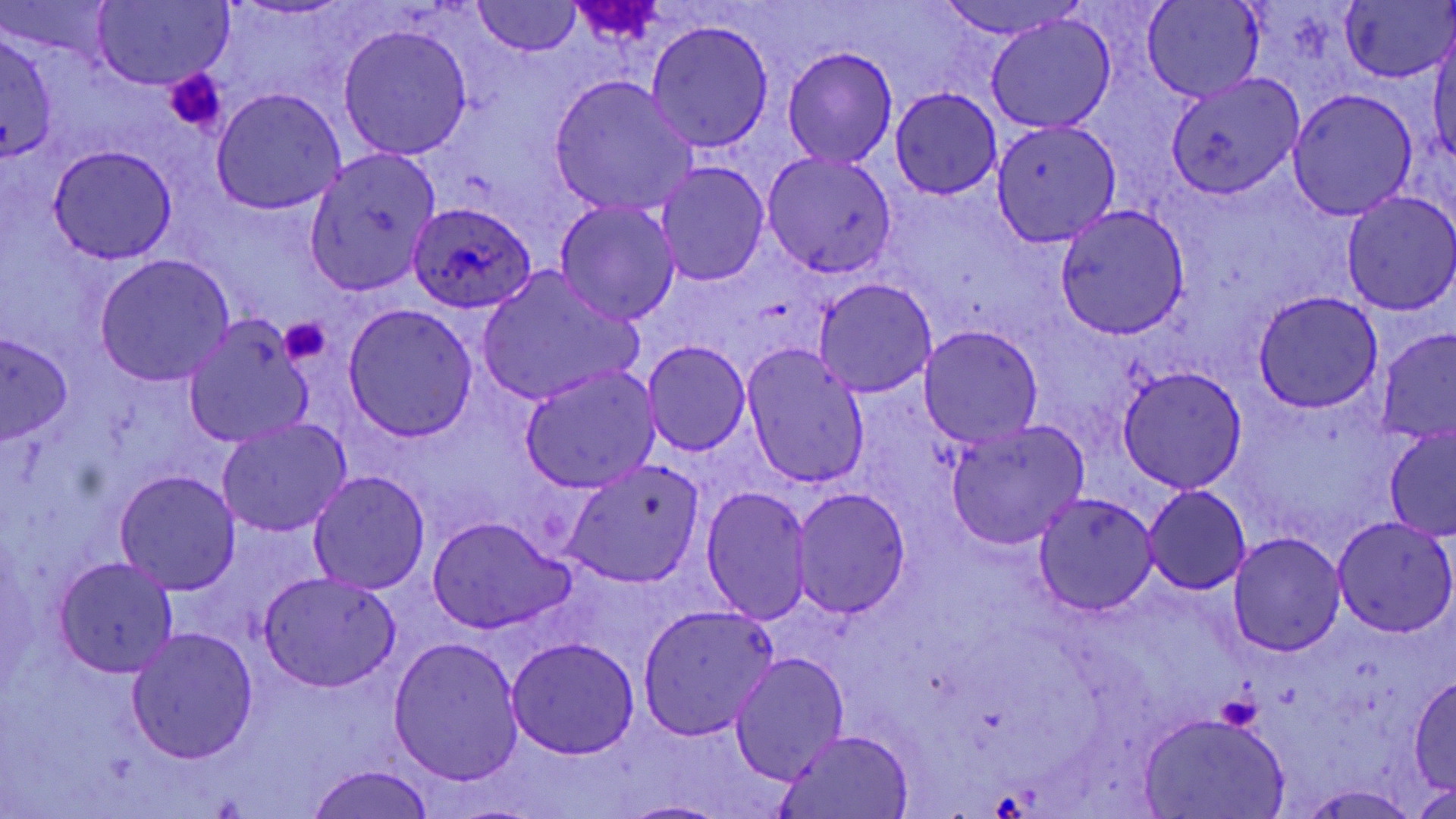

Summary:
  - Coordinate format: approximate bounding boxes as [x1, y1, x2, y2] in pixels
  - Plasmodium ovale-infected red blood cell locations: [406, 200, 537, 313]
  - Uninfected red blood cell locations: [2, 0, 115, 58], [1142, 0, 1263, 103], [1342, 0, 1454, 84], [935, 1, 1080, 38], [90, 2, 232, 88], [473, 2, 582, 58], [985, 14, 1116, 135], [647, 20, 773, 152], [338, 24, 472, 161], [1430, 29, 1456, 165], [0, 30, 59, 166], [782, 47, 898, 169], [1165, 71, 1306, 200], [550, 76, 697, 217], [211, 88, 346, 214], [891, 88, 1001, 199], [1287, 90, 1418, 221], [991, 118, 1120, 246], [51, 145, 175, 263], [303, 149, 441, 297], [763, 152, 898, 278], [655, 162, 770, 286], [1341, 191, 1456, 315], [553, 200, 681, 325], [1054, 206, 1189, 339], [94, 255, 233, 385], [478, 268, 641, 406], [814, 278, 937, 397], [1253, 291, 1384, 412], [342, 305, 477, 441], [184, 318, 314, 446], [920, 325, 1043, 447], [1377, 326, 1456, 446], [0, 331, 73, 443], [642, 341, 750, 457], [741, 345, 871, 492], [520, 365, 659, 493], [1117, 366, 1248, 494], [217, 418, 351, 538], [946, 422, 1087, 550], [1385, 426, 1456, 540], [563, 460, 704, 589], [116, 470, 241, 594], [308, 471, 430, 595], [701, 485, 810, 623], [1143, 485, 1251, 595], [792, 487, 911, 618], [1034, 493, 1158, 616], [427, 517, 573, 634], [1332, 517, 1455, 637], [1228, 534, 1346, 656], [53, 557, 178, 678], [259, 570, 401, 691], [636, 604, 780, 742], [125, 627, 259, 765], [388, 636, 524, 786], [506, 636, 641, 759], [730, 653, 848, 783], [1410, 677, 1455, 793], [1139, 713, 1291, 818], [775, 728, 918, 818], [306, 763, 438, 819], [1415, 782, 1455, 819], [1298, 785, 1422, 817], [616, 799, 726, 819]
  - Platelet locations: [572, 1, 664, 45], [165, 69, 226, 134], [279, 316, 333, 365], [1217, 692, 1264, 732]
  - Slide-level diagnosis: Plasmodium ovale
  - Stain: May-Grünwald-Giemsa
  - Modality: optical microscopy
  - Field of view: one of a larger specimen
  - Magnification: 1000x
  - Image size: 1456×819 pixels
  - Preparation: thin blood smear